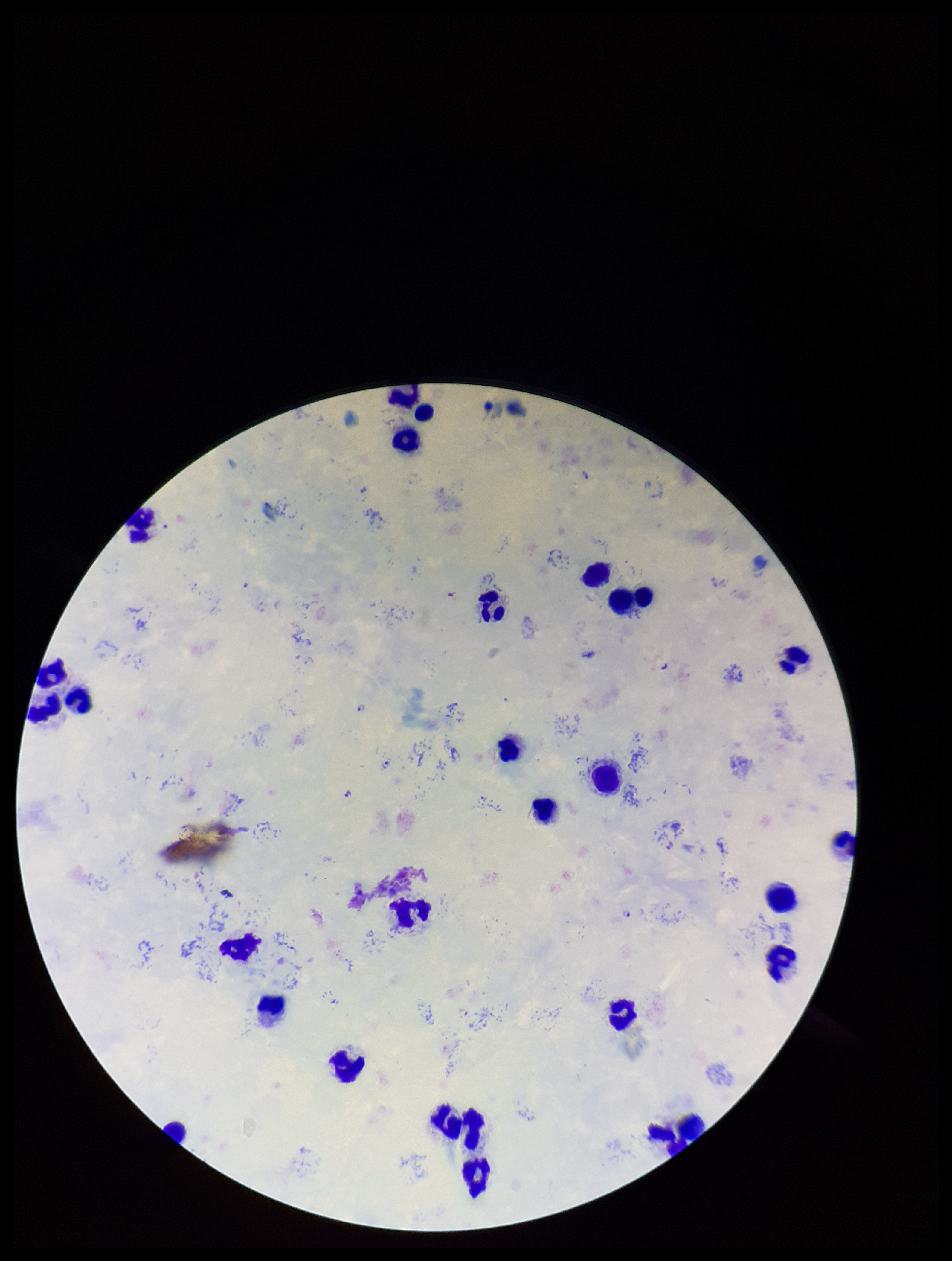 Photographed through the microscope eyepiece with a smartphone camera. Giemsa stain. Preparation: thick smear. Single field of view. Parasite count: 7. Species reported for this patient: Plasmodium falciparum. Plasmodium parasites: identified. Image is 952×1261 pixels. Patient malaria status: positive. Leukocyte count: 26.